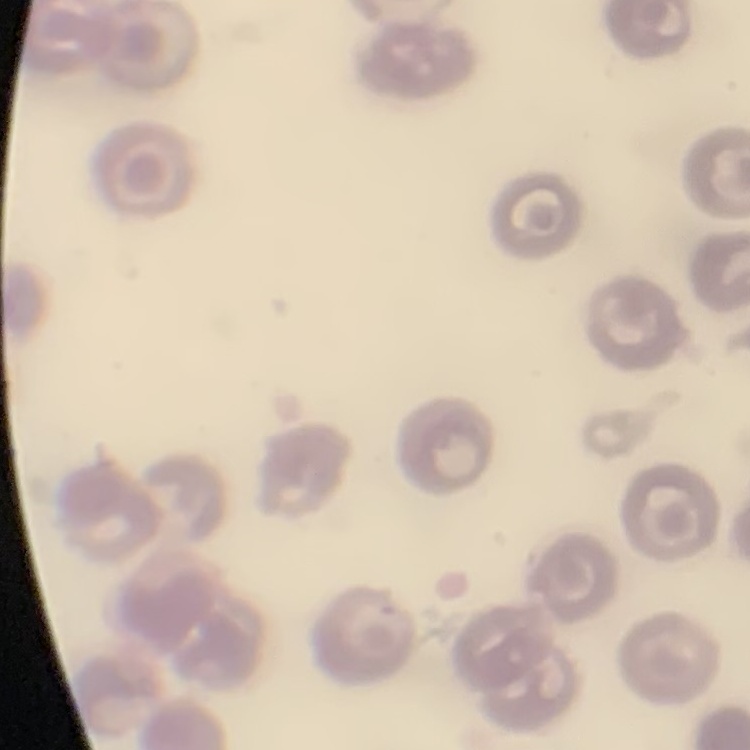

The erythrocytes show no rouleaux formation. Thin peripheral smear. Stained with either Field's or Giemsa. One tile cut from a larger photomicrograph.